Identify the blood parasite species.
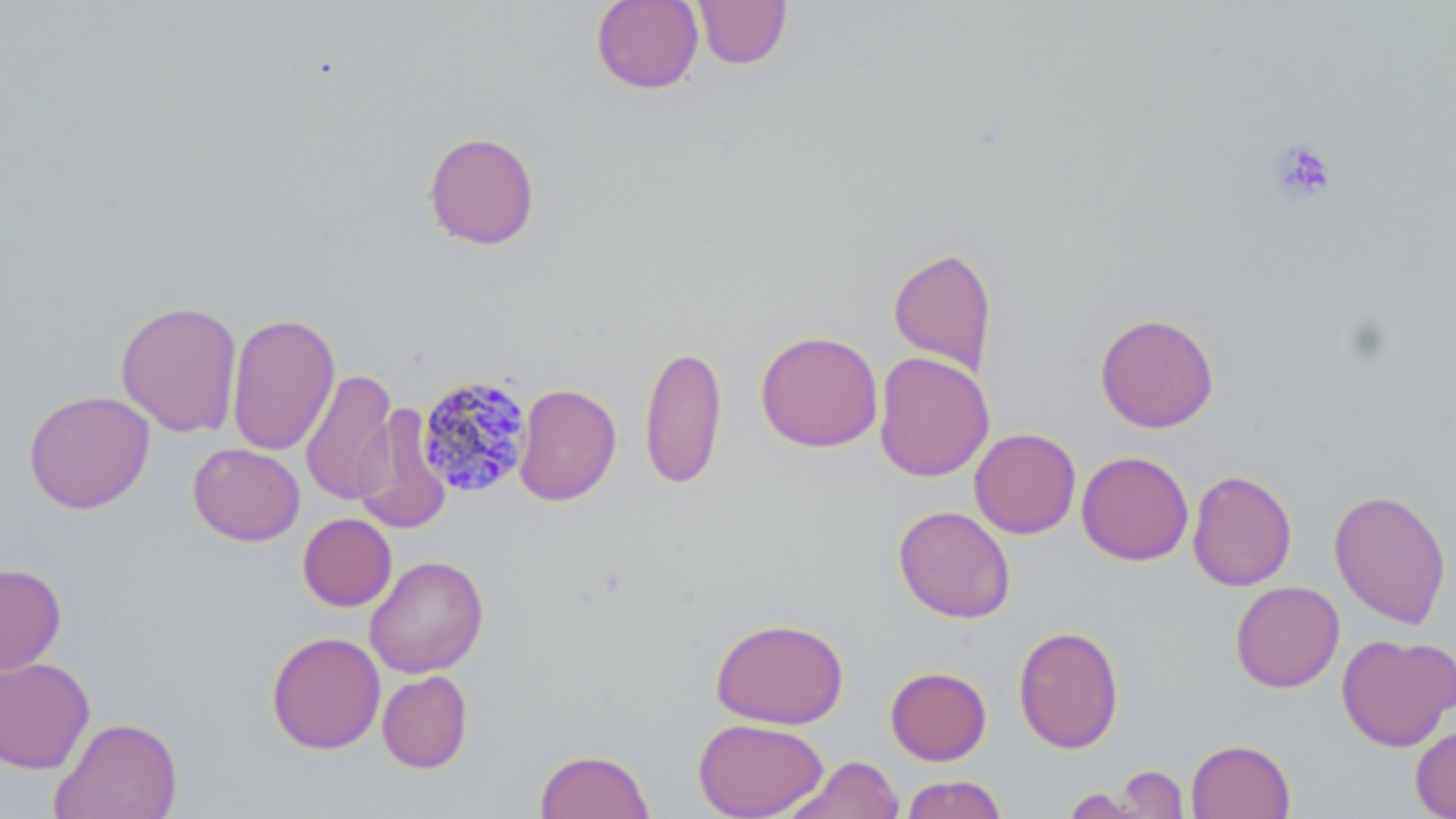
Plasmodium malariae.

Summary:
  - Coordinate format: approximate bounding boxes as [x1, y1, x2, y2] in pixels
  - Uninfected red blood cell locations: [591, 0, 704, 94], [692, 0, 792, 70], [422, 131, 541, 250], [888, 247, 997, 375], [115, 300, 243, 437], [227, 312, 340, 456], [1095, 312, 1219, 433], [755, 330, 884, 452], [639, 343, 728, 489], [873, 351, 995, 482], [301, 369, 398, 506], [513, 383, 621, 506], [23, 390, 155, 514], [352, 405, 452, 534], [969, 428, 1081, 539], [188, 443, 305, 546], [1076, 450, 1193, 566], [1187, 469, 1297, 591], [1329, 489, 1452, 628], [893, 505, 1016, 624], [298, 513, 397, 611], [365, 554, 489, 679], [0, 563, 67, 676], [1230, 580, 1345, 693], [710, 617, 849, 729], [1013, 625, 1125, 754], [266, 631, 386, 754], [1336, 633, 1455, 752], [0, 657, 95, 774], [885, 666, 992, 765], [376, 670, 473, 773], [49, 715, 183, 818], [693, 718, 828, 818], [1411, 723, 1456, 818], [1186, 739, 1296, 819], [535, 748, 654, 819], [786, 755, 903, 818], [1114, 765, 1189, 818], [901, 774, 1008, 819], [1060, 788, 1147, 818]
  - Plasmodium malariae-infected red blood cell locations: [416, 375, 533, 498]
  - Platelet locations: [1270, 139, 1336, 202]
  - Magnification: 1000x
  - Field of view: single
  - Modality: light microscopy
  - Image size: 1456×819 pixels
  - Stain: May-Grünwald-Giemsa
  - Preparation: thin blood film